Give the position of every Plasmodium parasite.
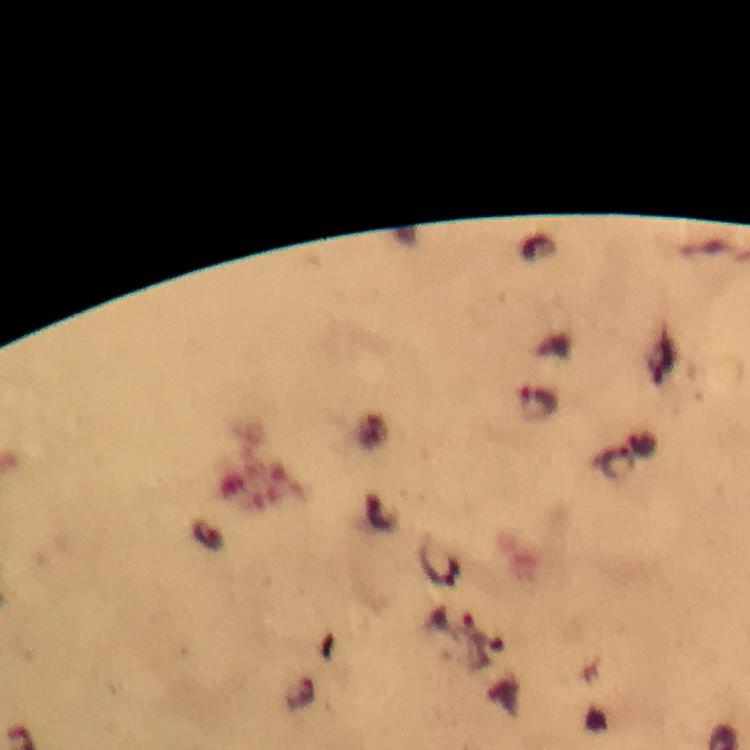

Approximate centers as (x, y) in pixels.
Plasmodium parasites: (539, 401), (451, 620).

context = from a diagnostic examination for malaria
preparation = thick blood smear
capture = smartphone mounted on the microscope
stain = Giemsa
image size = 750×750 pixels
magnification = 100x
cropped from = one field of view
immersion oil = applied